Report the malaria status of this cell.
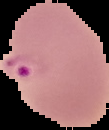

It is parasitized.

{
  "image_size": "109×130 pixels",
  "image_type": "cell region segmented out of the field of view; surrounding area masked to black",
  "preparation": "thin blood film"
}